Locate every Plasmodium parasite.
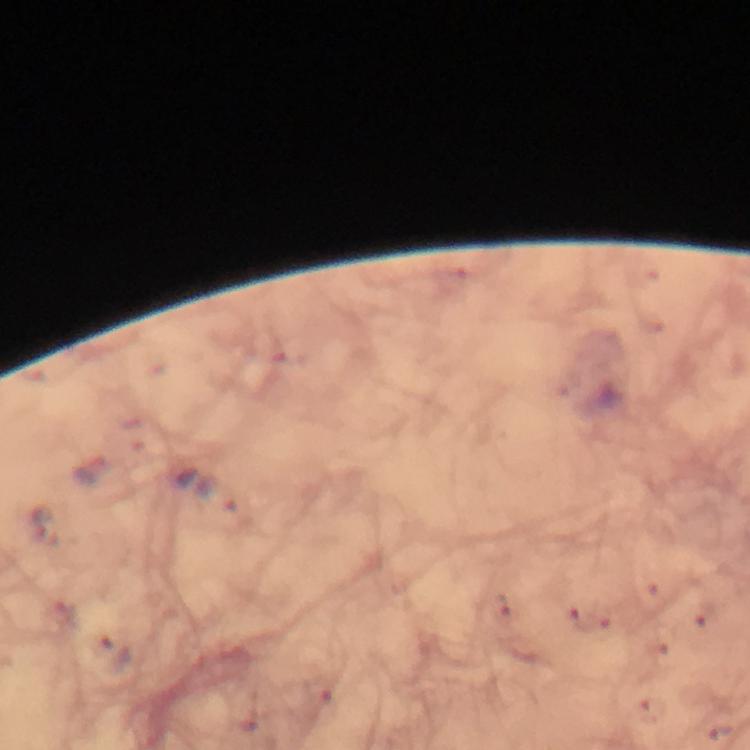

Approximate object centers, in pixels from the top-left corner.
Plasmodium parasites: (x=721, y=732).

immersion_oil: applied
preparation: thick blood film
cropped_from: one field of view
image_size: 750×750 pixels
capture: smartphone mounted on the microscope
context: from a diagnostic examination for malaria
magnification: 100x
stain: Giemsa